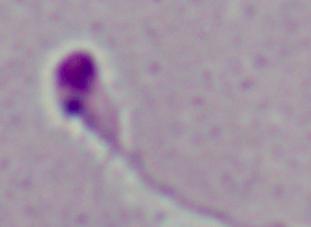 A Leishmania parasite is seen. Micrograph. Captured at 1000x magnification.